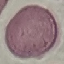

{
  "result": "no malaria parasites seen",
  "image_type": "cell patch, automatically extracted from a larger field of view and resized to 64 × 64 pixels",
  "preparation": "thin blood smear",
  "stain": "Giemsa",
  "capture": "smartphone camera at the microscope eyepiece"
}